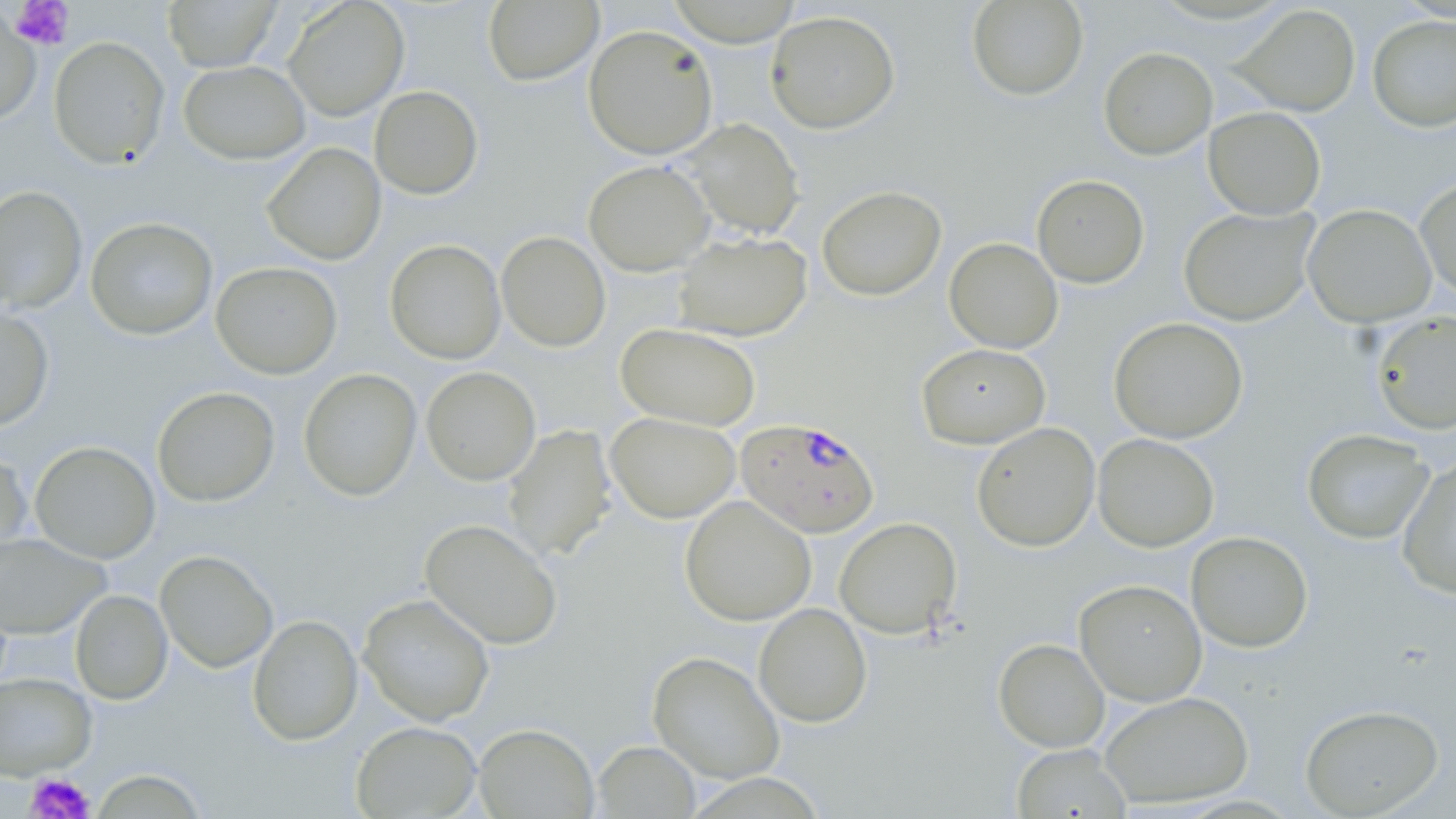

plasmodium_falciparum_infected_red_blood_cell_locations: 'approximate bounding boxes as (x1,y1)-(x2,y2) corner pairs in pixels: (735,418)-(880,538)'
slide_level_diagnosis: Plasmodium falciparum
modality: optical microscopy
stain: May-Grünwald-Giemsa
uninfected_red_blood_cell_locations: 'approximate bounding boxes as (x1,y1)-(x2,y2) corner pairs in pixels: (162,0)-(281,72), (966,0)-(1089,101), (283,1)-(409,121), (483,1)-(603,86), (666,2)-(804,46), (1233,4)-(1360,116), (0,5)-(41,126), (765,10)-(901,134), (1367,15)-(1456,131), (582,24)-(719,160), (48,36)-(170,169), (1098,46)-(1218,160), (179,60)-(310,164), (369,85)-(483,199), (1203,106)-(1326,220), (678,117)-(805,240), (262,142)-(386,266), (583,160)-(715,276), (1031,174)-(1149,288), (1414,176)-(1456,301), (0,185)-(87,314), (817,185)-(946,301), (1302,204)-(1437,328), (1179,206)-(1319,326), (85,217)-(218,340), (496,231)-(611,352), (672,232)-(812,341), (944,237)-(1063,354), (384,239)-(506,364), (211,261)-(342,379), (0,305)-(55,431), (1370,311)-(1456,435), (1108,317)-(1248,443), (616,323)-(761,430), (916,343)-(1050,449), (421,366)-(541,486), (298,368)-(421,502), (151,386)-(280,507), (605,412)-(740,523), (971,422)-(1100,552), (502,424)-(616,561), (1301,428)-(1435,544), (1093,433)-(1219,552), (29,441)-(161,563), (0,447)-(33,561), (1397,456)-(1456,599), (680,495)-(817,626), (834,516)-(962,638), (420,518)-(563,650), (1186,531)-(1313,652), (0,532)-(109,639), (154,550)-(278,673), (1074,579)-(1207,706), (70,589)-(172,705), (358,593)-(495,726), (753,603)-(872,727), (247,614)-(363,746), (994,638)-(1109,752), (648,651)-(785,784), (0,672)-(96,780), (1099,691)-(1254,809), (1299,703)-(1444,817), (350,721)-(481,818), (474,723)-(599,818), (593,740)-(700,818), (1011,744)-(1132,819), (88,768)-(211,818)'
image_size: 1456×819 pixels
preparation: thin blood smear
magnification: 1000x
platelet_locations: 'approximate bounding boxes as (x1,y1)-(x2,y2) corner pairs in pixels: (9,0)-(74,51), (24,772)-(96,818)'
field_of_view: one of a larger specimen